Name the parasite shown.
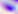

This is Toxoplasma gondii.

Captured at 400x magnification. Micrograph.